Locate and identify every blood parasite.
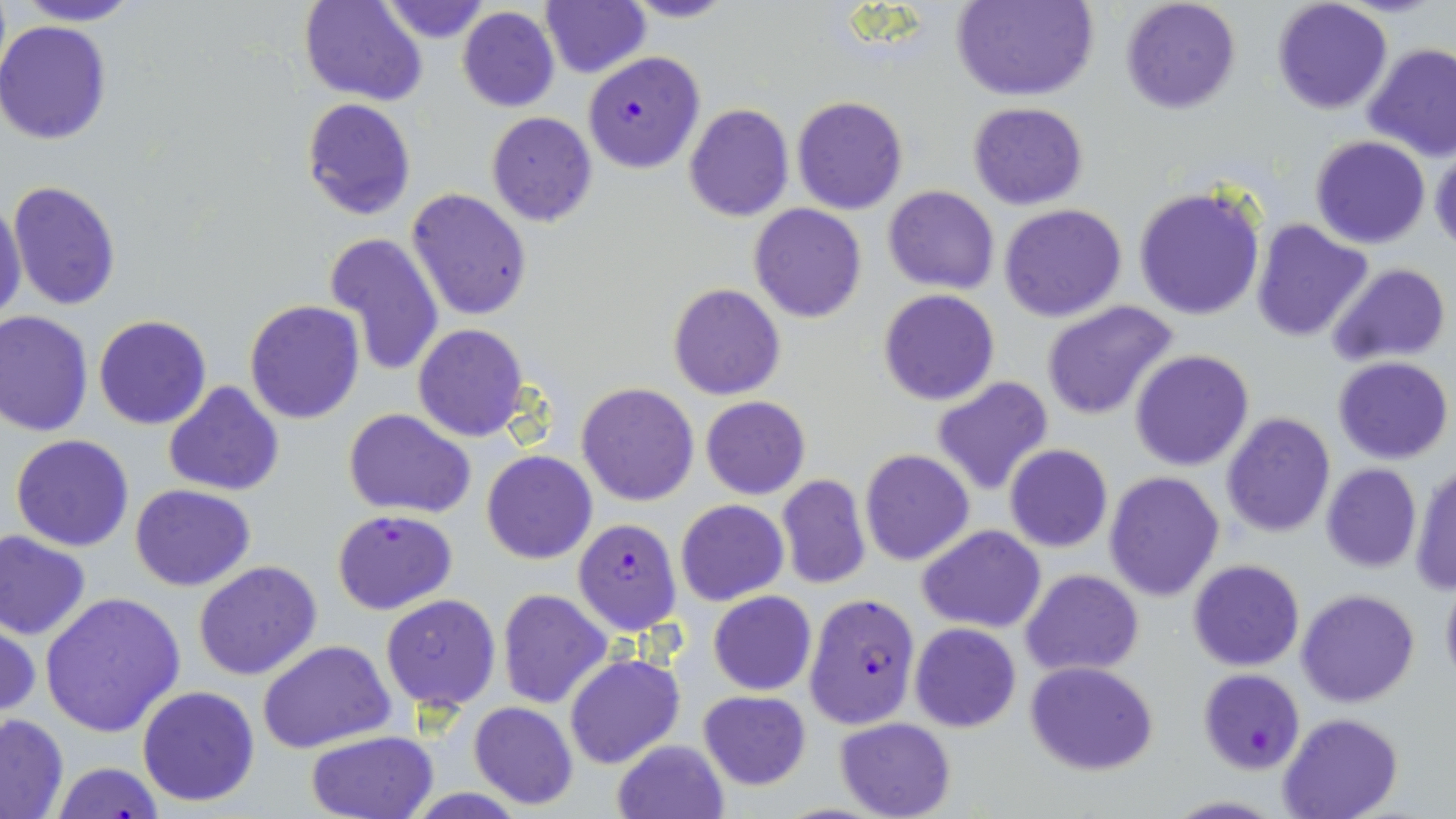

Approximate bounding boxes as named x1/y1/x2/y2 corners in pixels.
Plasmodium falciparum-infected red blood cells: (x1=581, y1=52, x2=706, y2=174), (x1=332, y1=507, x2=457, y2=614), (x1=572, y1=518, x2=682, y2=635), (x1=804, y1=593, x2=921, y2=730), (x1=1198, y1=669, x2=1305, y2=774).
No Plasmodium ovale, Plasmodium malariae, Plasmodium vivax, Babesia divergens, or Trypanosoma brucei observed.

slide-level diagnosis = Plasmodium falciparum
modality = optical microscopy
magnification = 1000x
image size = 1456×819 pixels
preparation = thin blood film
uninfected red blood cell locations = approximate bounding boxes as named x1/y1/x2/y2 corners in pixels: (x1=13, y1=0, x2=146, y2=26), (x1=300, y1=0, x2=427, y2=105), (x1=377, y1=0, x2=492, y2=44), (x1=616, y1=0, x2=739, y2=23), (x1=953, y1=0, x2=1098, y2=102), (x1=1120, y1=0, x2=1242, y2=116), (x1=1272, y1=0, x2=1394, y2=115), (x1=540, y1=2, x2=650, y2=77), (x1=458, y1=7, x2=559, y2=112), (x1=0, y1=20, x2=112, y2=144), (x1=1361, y1=42, x2=1456, y2=163), (x1=790, y1=96, x2=909, y2=215), (x1=301, y1=97, x2=416, y2=220), (x1=969, y1=101, x2=1089, y2=209), (x1=684, y1=103, x2=794, y2=221), (x1=486, y1=112, x2=597, y2=227), (x1=1309, y1=134, x2=1431, y2=248), (x1=1429, y1=146, x2=1456, y2=255), (x1=8, y1=179, x2=121, y2=313), (x1=1133, y1=184, x2=1267, y2=322), (x1=883, y1=185, x2=999, y2=294), (x1=407, y1=188, x2=530, y2=322), (x1=0, y1=197, x2=26, y2=320), (x1=999, y1=203, x2=1128, y2=322), (x1=750, y1=204, x2=867, y2=322), (x1=1251, y1=218, x2=1374, y2=343), (x1=323, y1=232, x2=446, y2=377), (x1=1326, y1=262, x2=1451, y2=367), (x1=668, y1=282, x2=786, y2=400), (x1=878, y1=289, x2=1000, y2=405), (x1=245, y1=300, x2=364, y2=424), (x1=1042, y1=301, x2=1179, y2=422), (x1=0, y1=309, x2=94, y2=437), (x1=94, y1=315, x2=212, y2=429), (x1=413, y1=325, x2=528, y2=441), (x1=1130, y1=349, x2=1255, y2=471), (x1=1333, y1=356, x2=1453, y2=464), (x1=930, y1=375, x2=1056, y2=496), (x1=163, y1=380, x2=285, y2=495), (x1=575, y1=382, x2=699, y2=505), (x1=702, y1=395, x2=810, y2=499), (x1=343, y1=408, x2=476, y2=517), (x1=1222, y1=410, x2=1335, y2=537), (x1=10, y1=434, x2=134, y2=551), (x1=1005, y1=443, x2=1113, y2=552), (x1=859, y1=449, x2=975, y2=566), (x1=481, y1=450, x2=597, y2=565), (x1=1408, y1=460, x2=1456, y2=596), (x1=1320, y1=463, x2=1421, y2=572), (x1=1103, y1=472, x2=1226, y2=601), (x1=776, y1=475, x2=872, y2=590), (x1=130, y1=484, x2=256, y2=591), (x1=676, y1=499, x2=789, y2=605), (x1=917, y1=524, x2=1045, y2=632), (x1=0, y1=529, x2=92, y2=641), (x1=1189, y1=559, x2=1304, y2=671), (x1=193, y1=561, x2=322, y2=681), (x1=1021, y1=568, x2=1144, y2=677), (x1=1439, y1=573, x2=1456, y2=691), (x1=1296, y1=588, x2=1420, y2=708), (x1=497, y1=589, x2=612, y2=710), (x1=708, y1=590, x2=816, y2=695), (x1=37, y1=591, x2=186, y2=738), (x1=380, y1=593, x2=502, y2=712), (x1=1, y1=618, x2=41, y2=721), (x1=909, y1=623, x2=1022, y2=733), (x1=257, y1=640, x2=395, y2=754), (x1=564, y1=653, x2=685, y2=770), (x1=1024, y1=660, x2=1159, y2=775), (x1=136, y1=684, x2=261, y2=807), (x1=697, y1=689, x2=812, y2=791), (x1=469, y1=701, x2=578, y2=809), (x1=0, y1=711, x2=69, y2=818), (x1=1276, y1=713, x2=1402, y2=819), (x1=833, y1=717, x2=956, y2=819), (x1=305, y1=732, x2=441, y2=819), (x1=611, y1=738, x2=729, y2=819), (x1=51, y1=762, x2=166, y2=819), (x1=1161, y1=795, x2=1287, y2=818)
field of view = single
stain = May-Grünwald-Giemsa